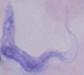
Photomicrograph. Captured at 1000x magnification. A trypanosome is shown.